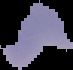

malaria_status: parasitized
image_size: 73×70 pixels
image_type: cell region segmented out of the field of view; surrounding area masked to black
preparation: thin blood film